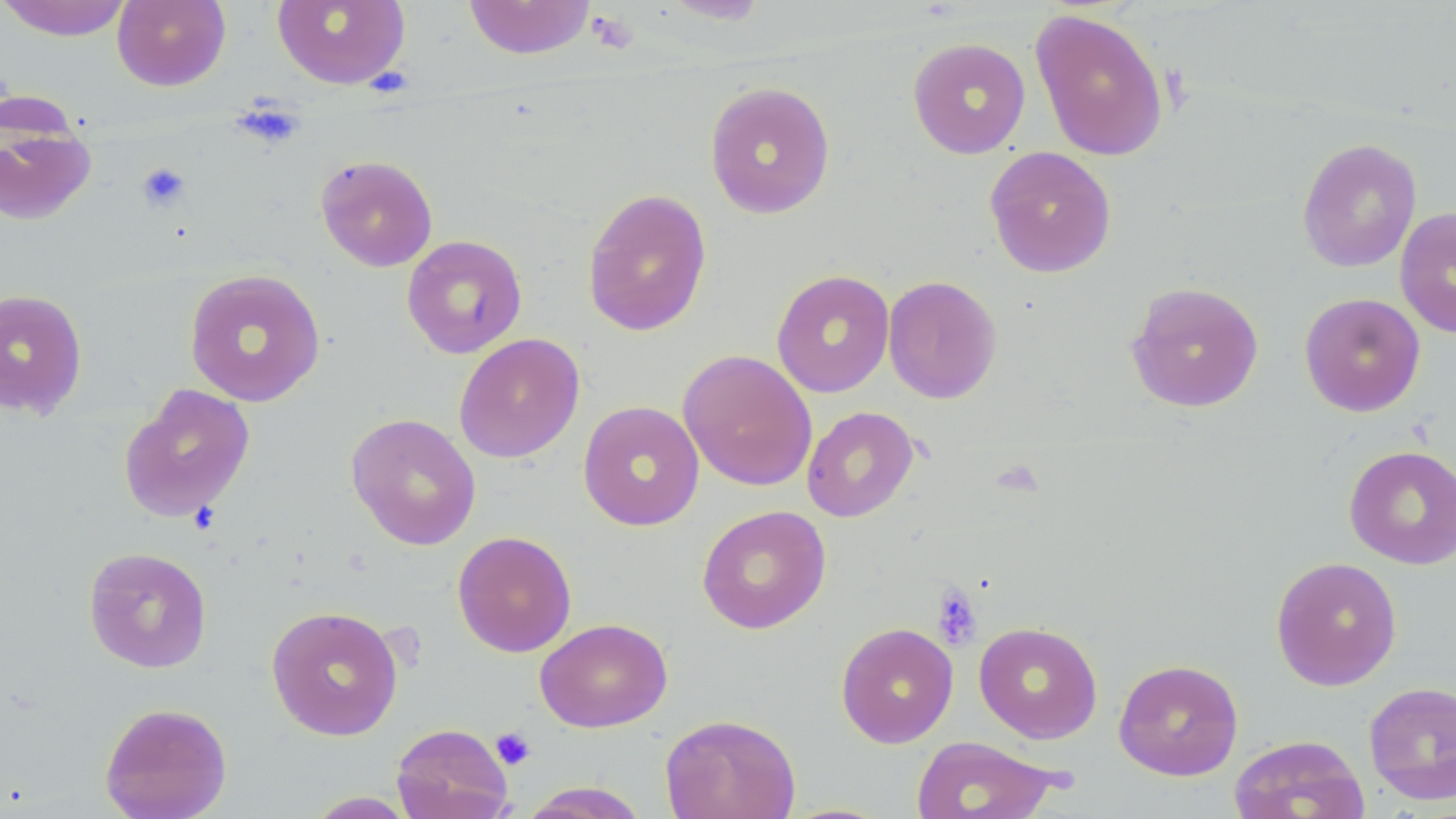
slide-level diagnosis = no evidence of blood parasites
stain = May-Grünwald-Giemsa
modality = light microscopy
uninfected red blood cell locations = approximate bounding boxes as (x1,y1)-(x2,y2) corner pairs in pixels: (0,0)-(134,41), (112,0)-(231,91), (272,0)-(410,89), (463,0)-(596,60), (661,0)-(770,24), (1030,8)-(1169,161), (907,37)-(1031,159), (704,80)-(836,219), (0,115)-(96,226), (1297,137)-(1422,273), (984,146)-(1117,278), (316,154)-(438,272), (581,188)-(712,336), (1395,206)-(1456,339), (401,235)-(527,359), (183,268)-(326,408), (771,268)-(895,398), (882,275)-(1002,404), (1125,281)-(1265,413), (0,288)-(88,419), (1299,292)-(1426,417), (453,333)-(585,463), (677,349)-(818,491), (118,383)-(256,523), (577,400)-(705,531), (802,406)-(919,523), (345,412)-(482,550), (1344,445)-(1456,569), (696,504)-(831,634), (452,530)-(577,657), (83,547)-(212,673), (1271,555)-(1402,690), (265,605)-(403,741), (535,617)-(672,733), (835,622)-(959,748), (974,622)-(1103,743), (1113,658)-(1244,780), (1363,680)-(1456,806), (99,702)-(232,819), (660,713)-(801,819), (391,723)-(513,819), (1228,734)-(1371,819), (911,735)-(1062,819), (519,782)-(651,818), (303,791)-(418,818)
platelet locations = approximate bounding boxes as (x1,y1)-(x2,y2) corner pairs in pixels: (587,11)-(638,54), (232,98)-(304,150), (136,162)-(191,213), (931,584)-(983,651), (491,727)-(536,770)
preparation = thin blood film
magnification = 1000x
image size = 1456×819 pixels
field of view = one of a larger specimen